Point out each Plasmodium parasite.
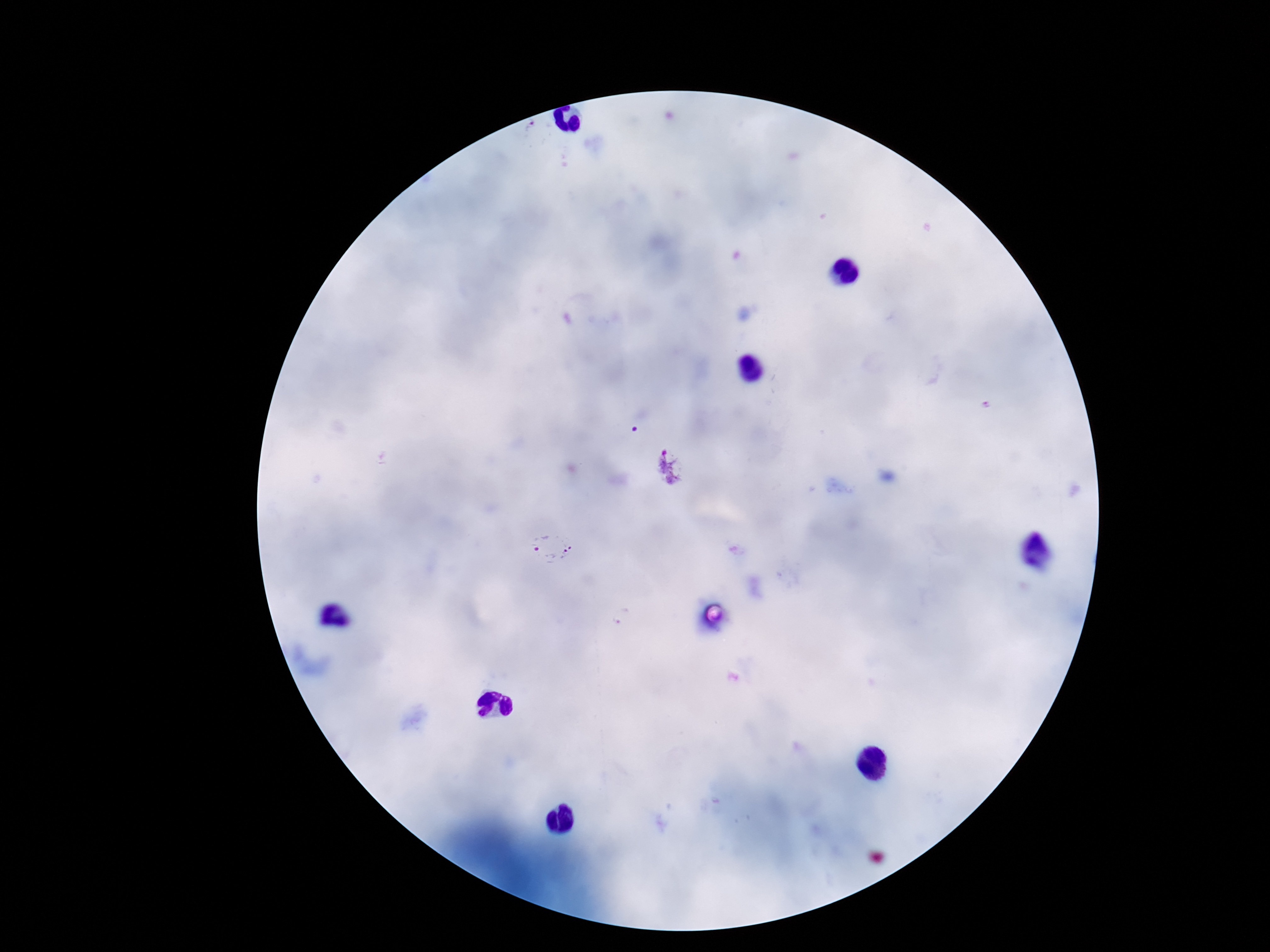
Approximate centers as (x, y) in pixels.
Plasmodium parasites: (668, 468), (550, 550).

Summary:
  - Stain: Giemsa
  - Capture: smartphone camera through the microscope eyepiece
  - Patient malaria status: infected
  - Magnification: 100x
  - Field of view: single
  - Preparation: thick peripheral-blood smear
  - Image size: 1270×952 pixels